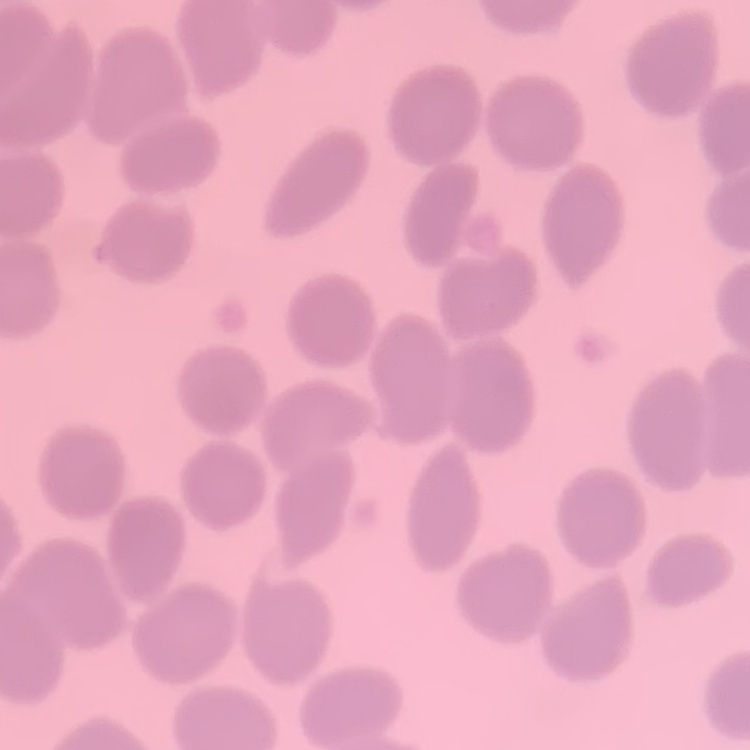
red blood cell morphology = no rouleaux formation
stain = Field's or Giemsa
preparation = thin blood film
image type = square crop of a larger photomicrograph